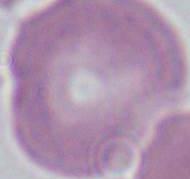
Summary:
  - Magnification: 1000x
  - Identification: erythrocyte
  - Modality: photomicrograph